Identify the preparation type.
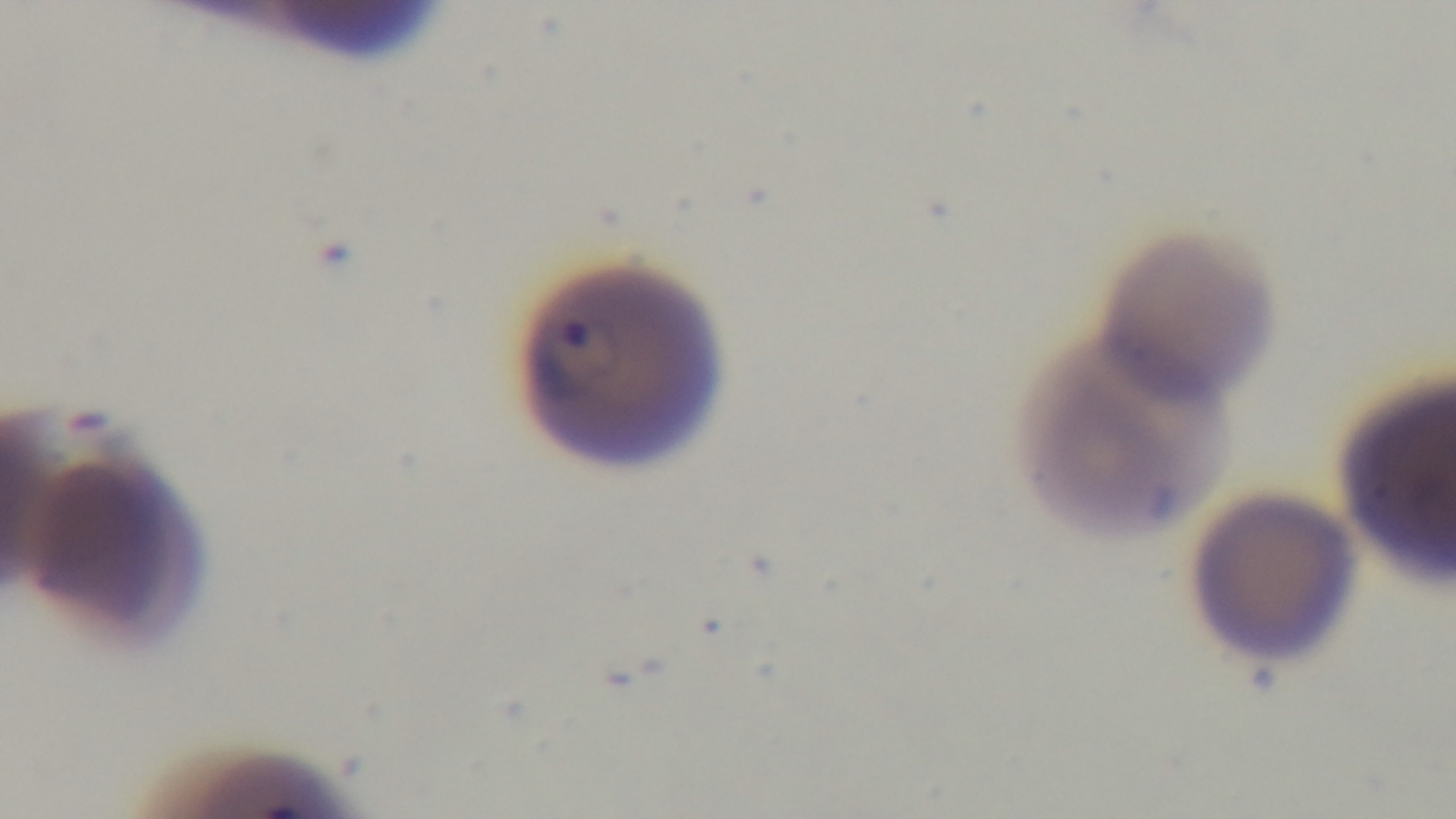

It is a thin blood film.

Captured with a mounted 4K digital camera. Giemsa-stained. One field from the slide. Light microscopy. Malaria status: positive. Oil-immersion objective, 100x.